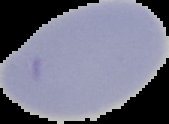
Segmented cell region on a black background. Image is 169×124 pixels. From a thin blood smear. Result: no malaria parasites detected.